Identify the parasite.
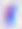
This is Toxoplasma gondii.

400x magnification. Micrograph.